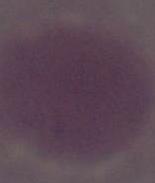
magnification = 1000x
identification = red blood cell
modality = photomicrograph